Name the blood parasite species.
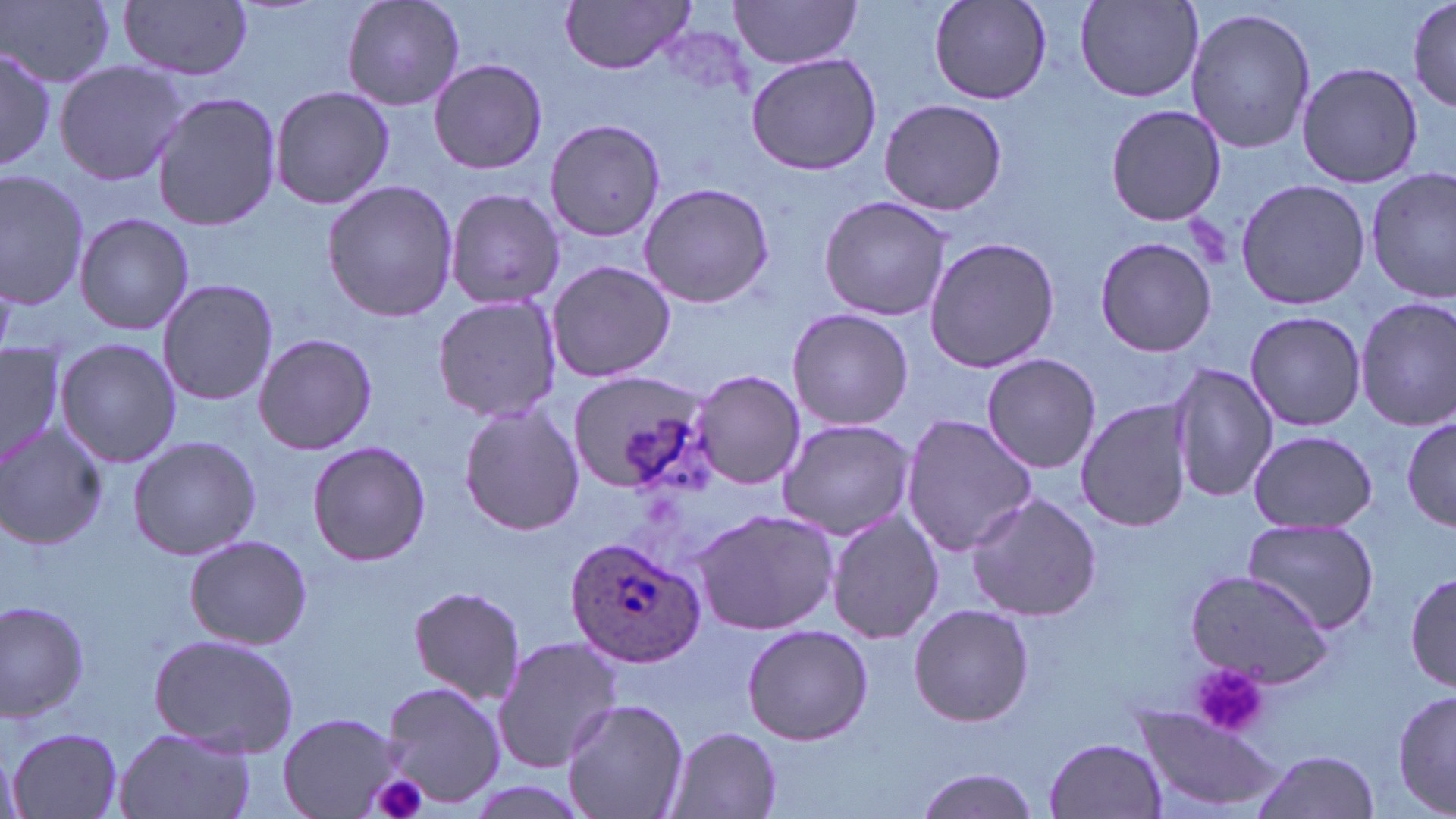

Plasmodium ovale.

Approximate bounding boxes as named x1/y1/x2/y2 corners in pixels. Uninfected red blood cell locations: (x1=121, y1=0, x2=252, y2=80), (x1=340, y1=0, x2=463, y2=110), (x1=1407, y1=0, x2=1455, y2=114), (x1=3, y1=1, x2=117, y2=89), (x1=561, y1=1, x2=697, y2=73), (x1=732, y1=1, x2=863, y2=70), (x1=928, y1=1, x2=1051, y2=104), (x1=1074, y1=1, x2=1204, y2=101), (x1=1184, y1=6, x2=1318, y2=155), (x1=0, y1=44, x2=56, y2=171), (x1=746, y1=52, x2=883, y2=174), (x1=54, y1=58, x2=188, y2=186), (x1=428, y1=60, x2=547, y2=174), (x1=1296, y1=62, x2=1424, y2=189), (x1=267, y1=85, x2=396, y2=209), (x1=150, y1=92, x2=282, y2=231), (x1=877, y1=97, x2=1008, y2=217), (x1=1104, y1=104, x2=1227, y2=226), (x1=544, y1=118, x2=667, y2=243), (x1=1, y1=168, x2=90, y2=311), (x1=1367, y1=168, x2=1455, y2=303), (x1=1235, y1=177, x2=1370, y2=311), (x1=321, y1=178, x2=460, y2=323), (x1=639, y1=182, x2=774, y2=308), (x1=443, y1=187, x2=565, y2=311), (x1=817, y1=195, x2=954, y2=320), (x1=74, y1=212, x2=195, y2=336), (x1=1093, y1=235, x2=1216, y2=357), (x1=923, y1=236, x2=1061, y2=373), (x1=545, y1=258, x2=676, y2=384), (x1=157, y1=278, x2=279, y2=407), (x1=431, y1=292, x2=561, y2=425), (x1=1352, y1=296, x2=1456, y2=430), (x1=786, y1=307, x2=914, y2=430), (x1=1242, y1=310, x2=1367, y2=431), (x1=253, y1=332, x2=377, y2=455), (x1=55, y1=337, x2=183, y2=467), (x1=1, y1=343, x2=67, y2=471), (x1=981, y1=353, x2=1100, y2=472), (x1=1168, y1=361, x2=1278, y2=504), (x1=691, y1=369, x2=804, y2=490), (x1=568, y1=371, x2=714, y2=496), (x1=1074, y1=397, x2=1193, y2=532), (x1=456, y1=403, x2=586, y2=537), (x1=899, y1=413, x2=1036, y2=557), (x1=1403, y1=415, x2=1456, y2=535), (x1=776, y1=419, x2=917, y2=539), (x1=0, y1=424, x2=108, y2=550), (x1=1246, y1=430, x2=1379, y2=532), (x1=127, y1=435, x2=261, y2=561), (x1=307, y1=442, x2=433, y2=567), (x1=963, y1=491, x2=1103, y2=622), (x1=694, y1=507, x2=840, y2=635), (x1=824, y1=509, x2=945, y2=645), (x1=1242, y1=517, x2=1382, y2=638), (x1=183, y1=534, x2=312, y2=649), (x1=1182, y1=571, x2=1334, y2=687), (x1=1407, y1=572, x2=1456, y2=693), (x1=408, y1=585, x2=525, y2=705), (x1=0, y1=602, x2=90, y2=720), (x1=908, y1=603, x2=1034, y2=728), (x1=741, y1=625, x2=874, y2=745), (x1=148, y1=632, x2=302, y2=755), (x1=491, y1=633, x2=623, y2=773), (x1=377, y1=678, x2=508, y2=810), (x1=1391, y1=684, x2=1455, y2=819), (x1=560, y1=698, x2=690, y2=819), (x1=1133, y1=709, x2=1288, y2=816), (x1=278, y1=712, x2=407, y2=818), (x1=115, y1=724, x2=260, y2=819), (x1=8, y1=725, x2=124, y2=817), (x1=667, y1=725, x2=782, y2=818), (x1=1045, y1=736, x2=1168, y2=818), (x1=1, y1=743, x2=26, y2=819), (x1=1249, y1=750, x2=1383, y2=819), (x1=910, y1=766, x2=1042, y2=819). Plasmodium ovale-infected red blood cell locations: (x1=564, y1=534, x2=705, y2=667). Platelet locations: (x1=1189, y1=661, x2=1271, y2=739), (x1=371, y1=772, x2=430, y2=819). One field of a larger specimen. Thin blood smear. Image is 1456×819 pixels. May-Grünwald-Giemsa stain. Light microscopy. 1000x magnification.